Give the position of every Plasmodium parasite.
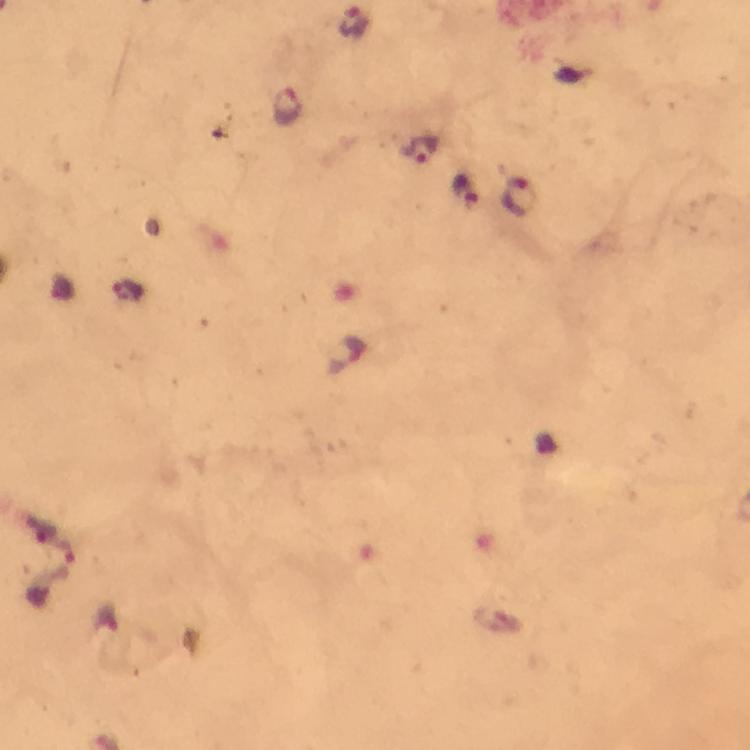
Approximate object centers, in pixels from the top-left corner.
Plasmodium parasites: (x=355, y=21), (x=287, y=105), (x=421, y=152), (x=467, y=189), (x=520, y=196).

From a diagnostic examination for malaria. Giemsa stain. Thick blood film. Cropped region of a single field of view. Immersion oil was used. Photographed with a smartphone mounted on the microscope. Image is 750×750 pixels. 100x magnification.